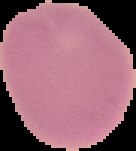

Image is 136×151 pixels. The area outside the segmented cell region is set to black. Result: no Plasmodium parasites detected. From a thin blood film.